Outline each white blood cell.
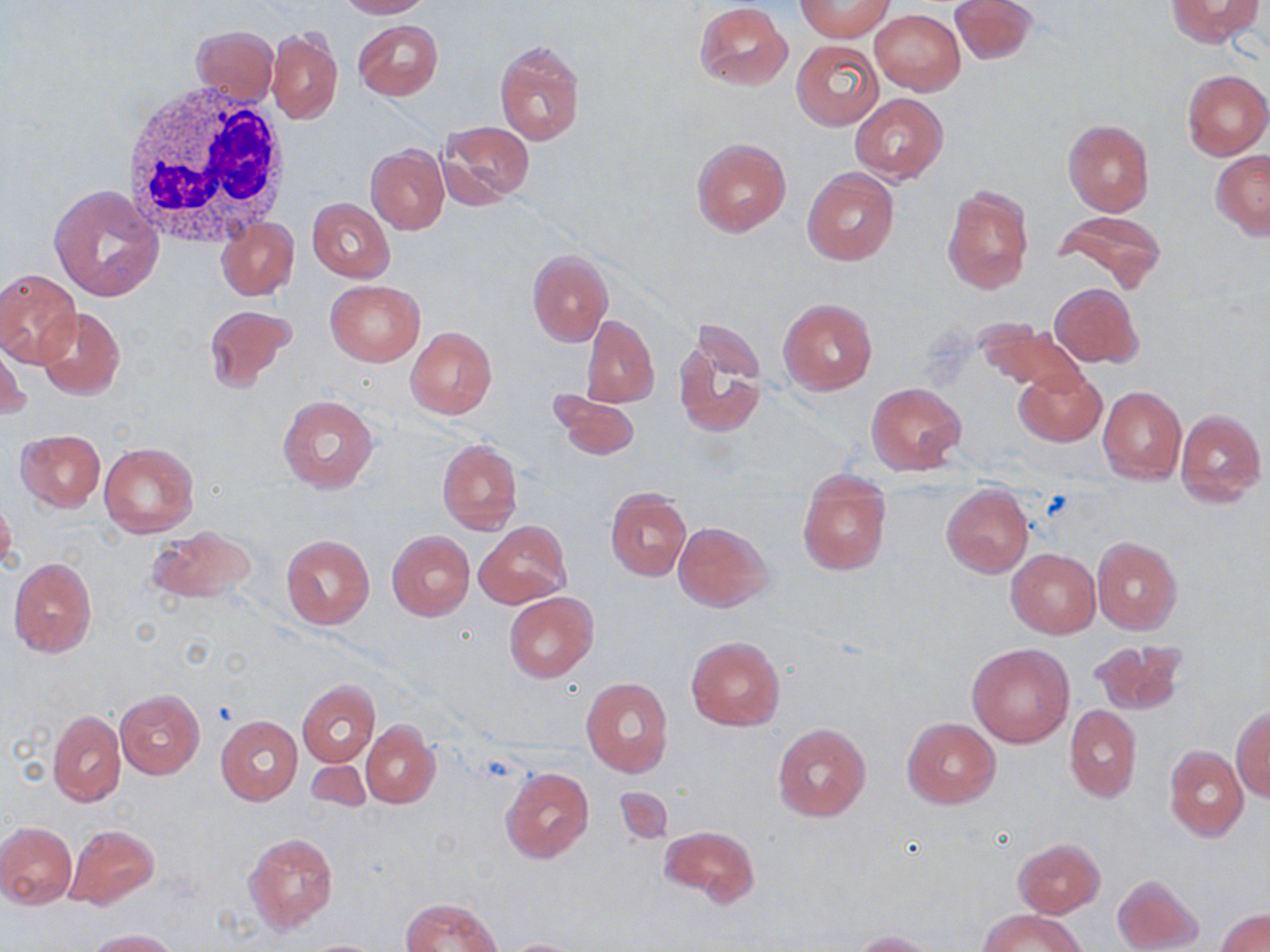
Approximate bounding boxes as named x1/y1/x2/y2 corners in pixels.
White blood cells: (x1=119, y1=82, x2=295, y2=251).

slide-level diagnosis = no evidence of blood parasites
magnification = 1000x
modality = optical microscopy
platelet locations = approximate bounding boxes as named x1/y1/x2/y2 corners in pixels: (x1=210, y1=702, x2=236, y2=728)
uninfected red blood cell locations = approximate bounding boxes as named x1/y1/x2/y2 corners in pixels: (x1=336, y1=0, x2=431, y2=18), (x1=949, y1=0, x2=1036, y2=66), (x1=1166, y1=0, x2=1263, y2=48), (x1=798, y1=1, x2=891, y2=40), (x1=694, y1=2, x2=792, y2=89), (x1=870, y1=10, x2=964, y2=94), (x1=353, y1=20, x2=442, y2=101), (x1=192, y1=25, x2=279, y2=104), (x1=267, y1=27, x2=343, y2=123), (x1=791, y1=39, x2=883, y2=130), (x1=494, y1=41, x2=586, y2=146), (x1=1182, y1=69, x2=1270, y2=160), (x1=850, y1=93, x2=947, y2=183), (x1=437, y1=120, x2=536, y2=204), (x1=1063, y1=120, x2=1155, y2=216), (x1=692, y1=138, x2=790, y2=235), (x1=366, y1=146, x2=449, y2=233), (x1=1211, y1=150, x2=1270, y2=238), (x1=802, y1=167, x2=899, y2=265), (x1=942, y1=183, x2=1034, y2=294), (x1=49, y1=185, x2=161, y2=302), (x1=308, y1=198, x2=394, y2=282), (x1=1052, y1=210, x2=1166, y2=294), (x1=217, y1=217, x2=298, y2=299), (x1=527, y1=250, x2=613, y2=346), (x1=0, y1=269, x2=81, y2=368), (x1=326, y1=280, x2=425, y2=366), (x1=1051, y1=283, x2=1142, y2=368), (x1=779, y1=298, x2=877, y2=394), (x1=204, y1=305, x2=298, y2=393), (x1=36, y1=307, x2=126, y2=401), (x1=581, y1=314, x2=659, y2=408), (x1=974, y1=320, x2=1085, y2=393), (x1=405, y1=325, x2=497, y2=420), (x1=673, y1=326, x2=766, y2=438), (x1=1, y1=341, x2=30, y2=424), (x1=1014, y1=368, x2=1105, y2=447), (x1=866, y1=383, x2=966, y2=474), (x1=1097, y1=386, x2=1186, y2=484), (x1=550, y1=390, x2=639, y2=460), (x1=277, y1=395, x2=378, y2=493), (x1=1175, y1=408, x2=1266, y2=505), (x1=15, y1=430, x2=104, y2=511), (x1=437, y1=439, x2=522, y2=535), (x1=99, y1=441, x2=199, y2=537), (x1=797, y1=469, x2=891, y2=575), (x1=941, y1=484, x2=1033, y2=577), (x1=606, y1=489, x2=691, y2=580), (x1=0, y1=493, x2=18, y2=578), (x1=474, y1=520, x2=571, y2=609), (x1=673, y1=521, x2=772, y2=612), (x1=145, y1=525, x2=260, y2=606), (x1=387, y1=530, x2=474, y2=620), (x1=281, y1=534, x2=374, y2=630), (x1=1092, y1=536, x2=1183, y2=635), (x1=1006, y1=549, x2=1099, y2=637), (x1=9, y1=558, x2=96, y2=658), (x1=503, y1=592, x2=597, y2=683), (x1=685, y1=636, x2=785, y2=731), (x1=1089, y1=639, x2=1187, y2=717), (x1=967, y1=643, x2=1075, y2=747), (x1=581, y1=676, x2=674, y2=777), (x1=298, y1=680, x2=380, y2=766), (x1=116, y1=690, x2=204, y2=779), (x1=1065, y1=705, x2=1142, y2=802), (x1=1232, y1=705, x2=1270, y2=801), (x1=48, y1=710, x2=125, y2=807), (x1=216, y1=716, x2=302, y2=804), (x1=901, y1=717, x2=1000, y2=808), (x1=361, y1=722, x2=439, y2=807), (x1=772, y1=722, x2=871, y2=822), (x1=1163, y1=746, x2=1249, y2=841), (x1=304, y1=757, x2=370, y2=812), (x1=500, y1=766, x2=594, y2=862), (x1=616, y1=786, x2=672, y2=844), (x1=0, y1=821, x2=77, y2=908), (x1=64, y1=824, x2=160, y2=910), (x1=660, y1=825, x2=760, y2=908), (x1=243, y1=831, x2=340, y2=934), (x1=1012, y1=838, x2=1105, y2=917), (x1=1112, y1=873, x2=1204, y2=952), (x1=401, y1=897, x2=503, y2=952), (x1=980, y1=908, x2=1085, y2=952), (x1=1216, y1=908, x2=1270, y2=952), (x1=85, y1=928, x2=180, y2=952), (x1=851, y1=930, x2=937, y2=952), (x1=498, y1=938, x2=591, y2=952), (x1=299, y1=939, x2=389, y2=951)
stain = May-Grünwald-Giemsa
field of view = single
image size = 1270×952 pixels
preparation = thin blood smear